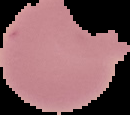

Summary:
  - Preparation: thin blood smear
  - Image type: segmented cell region on a black background
  - Image size: 130×115 pixels
  - Result: no Plasmodium parasites detected